Locate every leukocyte (white blood cell).
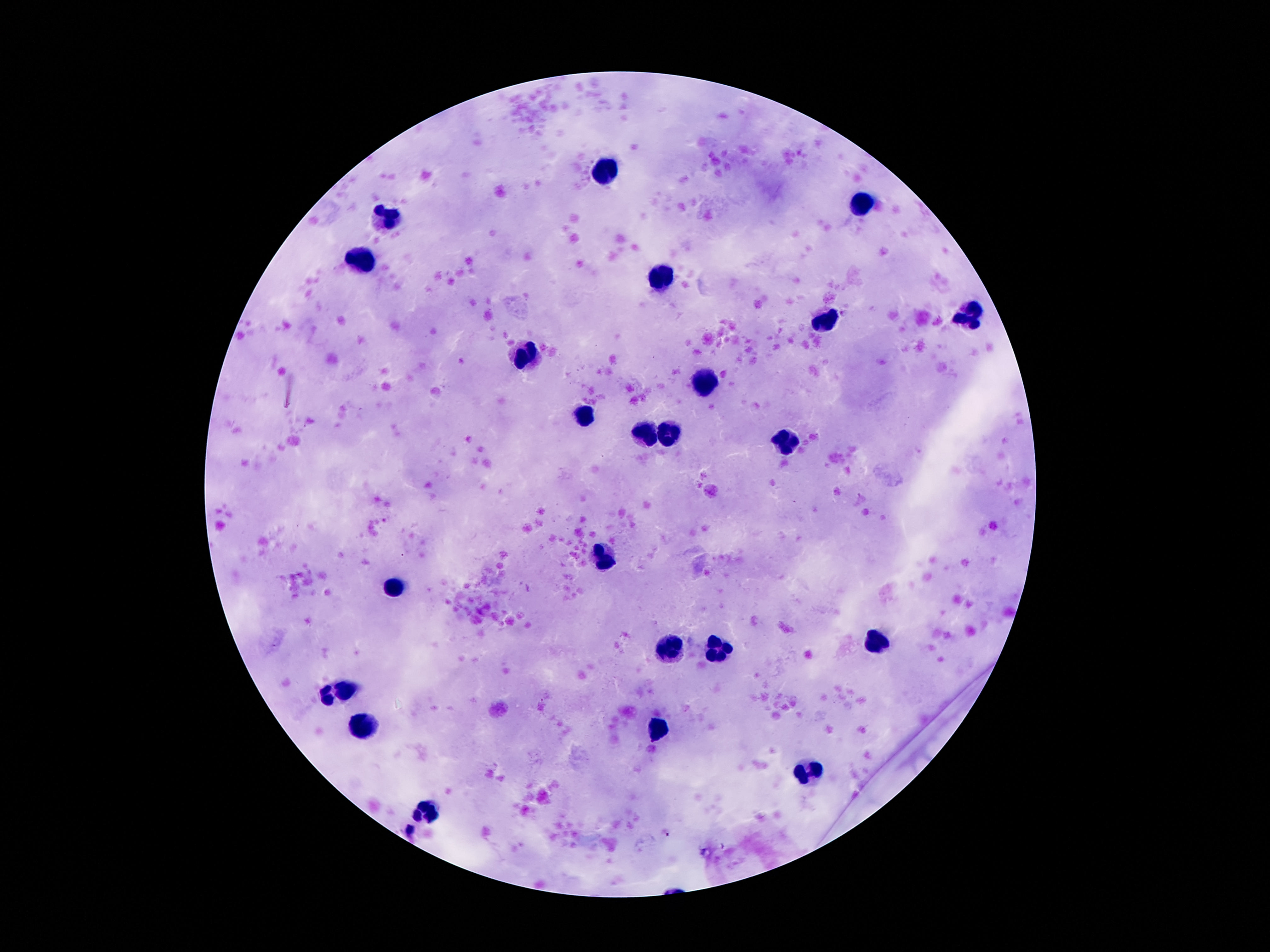

Approximate centers as [x, y] in pixels.
Leukocytes: [606, 169], [862, 204], [388, 214], [360, 260], [662, 273], [967, 318], [828, 319], [526, 359], [705, 384], [585, 415], [646, 432], [671, 434], [787, 443], [606, 555], [397, 588], [871, 641], [667, 648], [719, 650], [347, 685], [658, 727], [360, 729], [810, 772], [424, 809].

Image is 1270×952 pixels. One field from this slide. Smartphone photograph taken through the microscope eyepiece. Patient malaria status: negative. Giemsa stain. 100x magnification. Thick blood film.